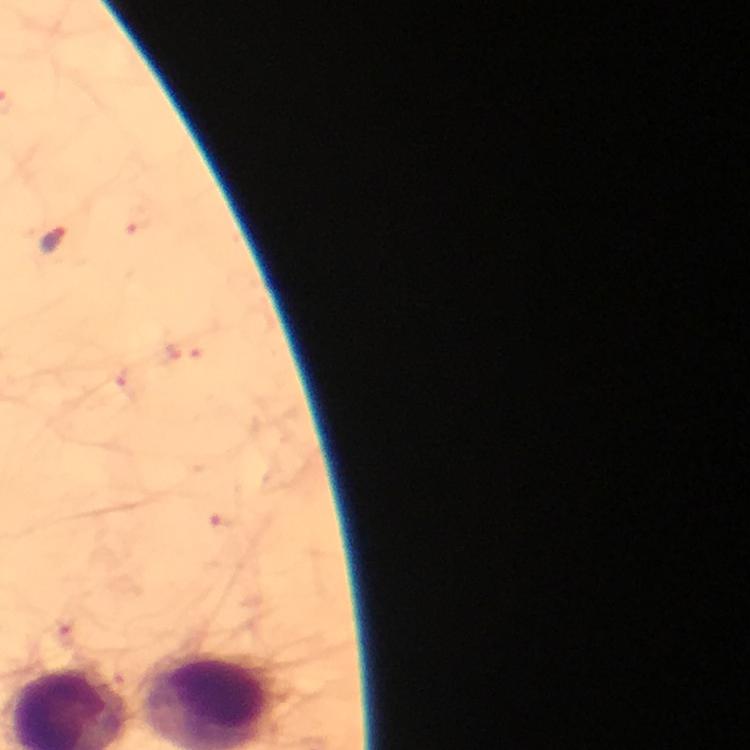

Approximate centers as [x, y] in pixels. Malaria parasite locations: [52, 239]. Thick smear. Photographed through the microscope with a smartphone camera. Giemsa stain. Immersion oil applied. At 100x magnification. Image is 750×750 pixels. From a malaria diagnostic workup. Cropped region of a single field of view.